Classify this cell by malaria status.
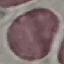
Uninfected.

Photographed with a smartphone camera at the microscope eyepiece. Giemsa stain. Thin blood smear. Cell patch, automatically extracted from a larger field of view and resized to 64 × 64 pixels.